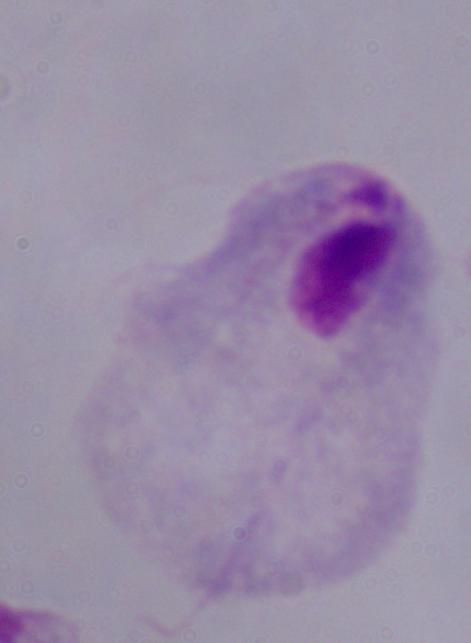

modality = photomicrograph
magnification = 1000x
identification = trichomonad